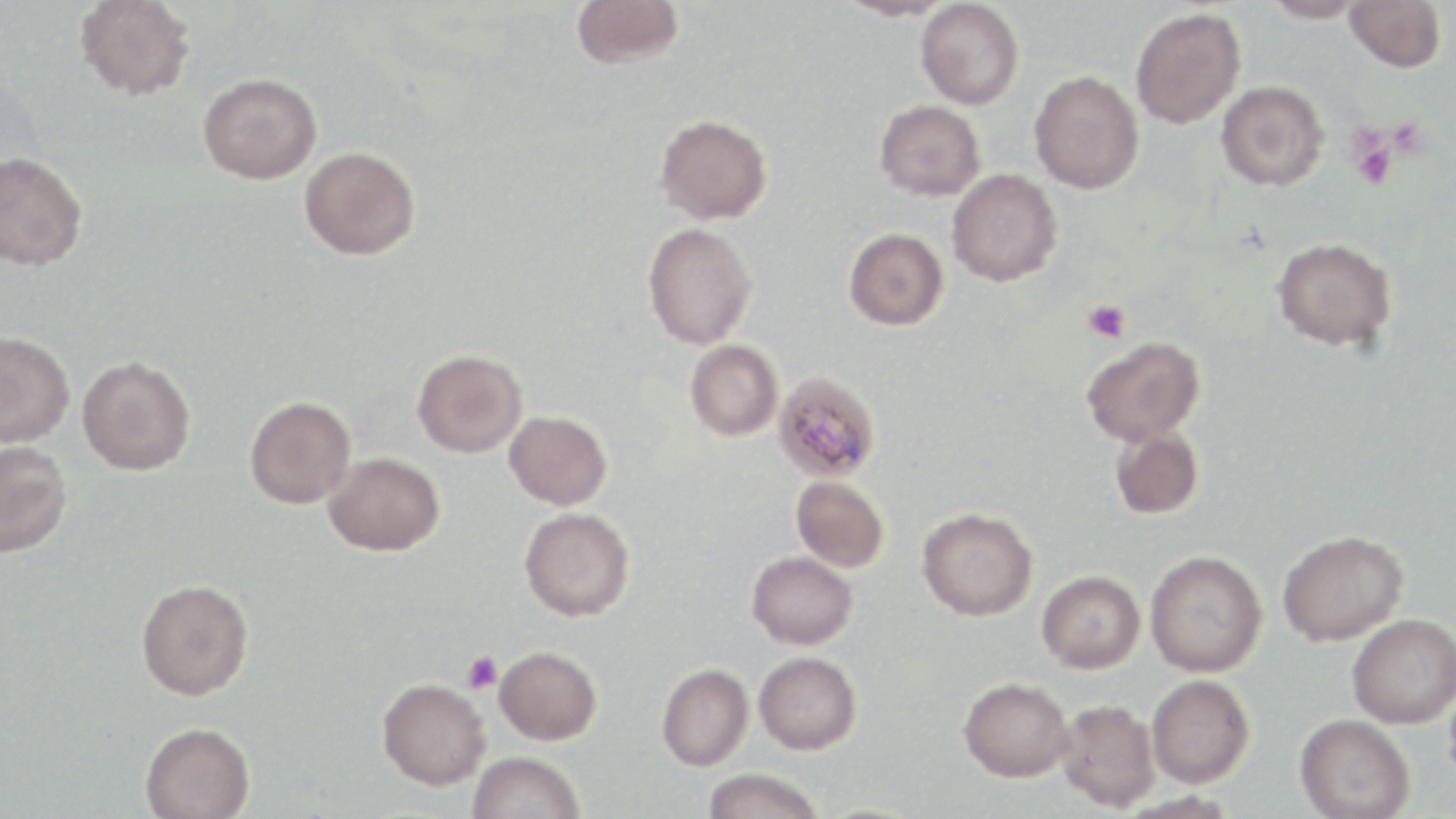

Summary:
  - Coordinate format: approximate bounding boxes as [x1, y1, x2, y2] in pixels
  - Platelet locations: [1348, 133, 1398, 189], [1083, 300, 1130, 344], [461, 651, 502, 694]
  - Plasmodium malariae-infected red blood cell locations: [773, 371, 882, 481]
  - Uninfected red blood cell locations: [75, 0, 195, 100], [571, 0, 684, 69], [834, 0, 954, 21], [1261, 0, 1367, 24], [1345, 0, 1446, 73], [916, 1, 1024, 110], [1130, 7, 1246, 129], [1029, 70, 1144, 194], [198, 72, 322, 184], [1216, 81, 1329, 191], [875, 100, 985, 201], [654, 113, 773, 225], [300, 146, 420, 260], [0, 151, 88, 271], [947, 168, 1063, 286], [642, 222, 757, 349], [844, 228, 948, 330], [1272, 236, 1396, 351], [0, 331, 75, 447], [1081, 335, 1205, 445], [685, 339, 783, 441], [412, 349, 527, 458], [77, 355, 195, 475], [244, 396, 356, 509], [504, 410, 612, 510], [1110, 426, 1204, 520], [0, 441, 72, 558], [323, 452, 445, 556], [790, 476, 889, 573], [519, 507, 635, 622], [917, 507, 1038, 620], [1277, 529, 1408, 646], [1145, 550, 1267, 677], [747, 551, 857, 650], [1037, 570, 1146, 673], [136, 579, 253, 701], [1347, 614, 1456, 728], [494, 646, 602, 745], [754, 651, 862, 754], [656, 663, 753, 771], [1444, 673, 1456, 796], [1146, 674, 1255, 788], [959, 676, 1073, 782], [377, 677, 490, 790], [1054, 698, 1161, 812], [1295, 714, 1416, 819], [140, 722, 255, 819], [468, 751, 584, 819], [702, 768, 826, 819]
  - Slide-level diagnosis: Plasmodium malariae
  - Stain: May-Grünwald-Giemsa
  - Modality: light microscopy
  - Magnification: 1000x
  - Preparation: thin blood smear
  - Image size: 1456×819 pixels
  - Field of view: one of a larger specimen